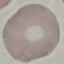

Malaria status: uninfected. Photographed with a smartphone camera at the microscope eyepiece. Thin blood smear. Giemsa stain. Automatically extracted cell patch, resized to 64 × 64 pixels.